Classify this cell by malaria status.
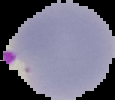
Parasitized.

image size = 115×100 pixels
preparation = thin blood smear
image type = segmented cell region on a black background